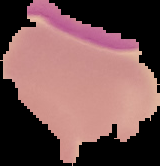 Image is 160×166 pixels. Cell region segmented out of the field of view; the surrounding area is masked to black. From a thin blood smear. Result: no malaria parasites seen.